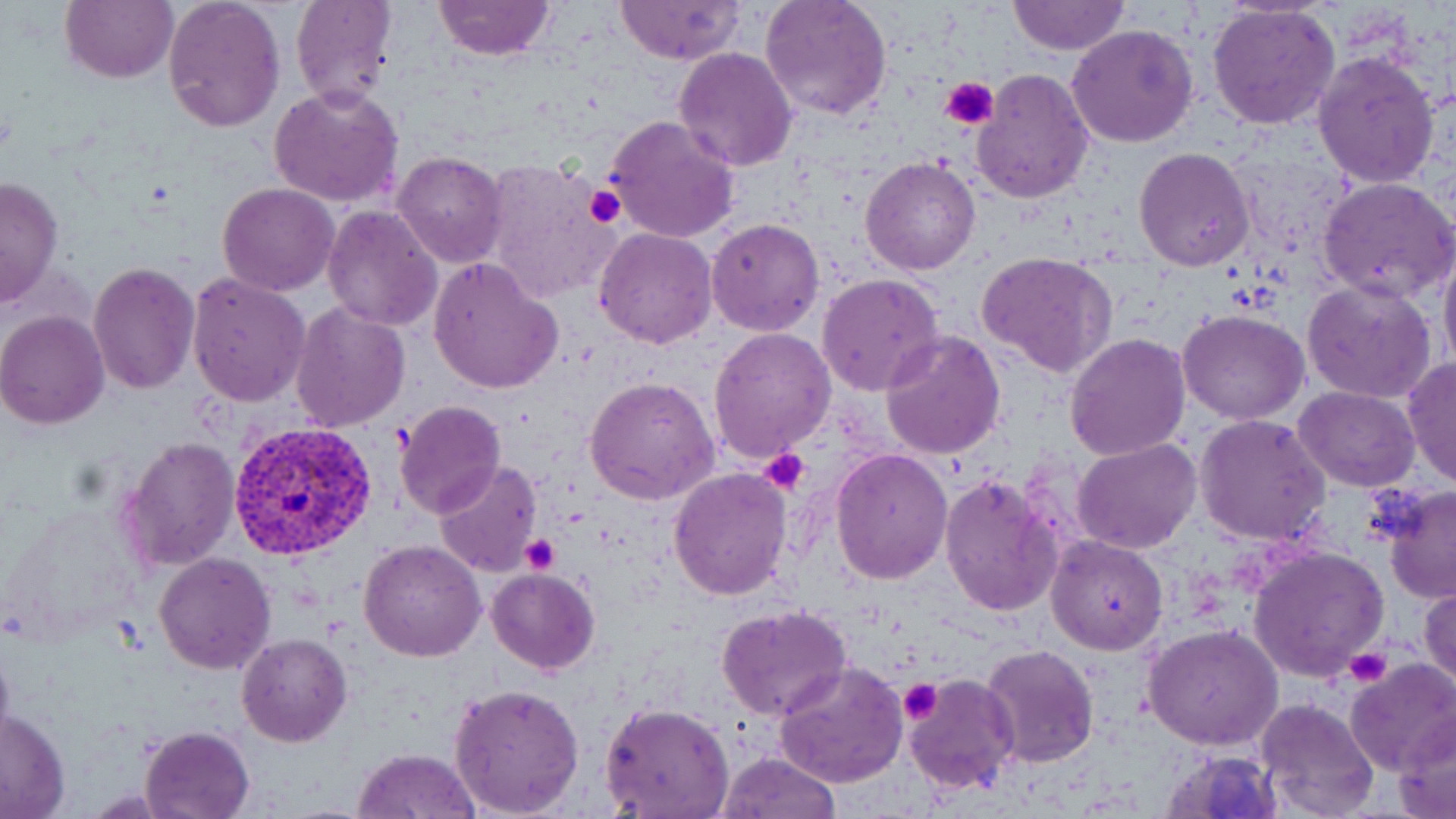

Approximate bounding boxes as (x1, y1, x2, y2) in pixels. Platelet locations: (941, 76, 996, 127), (585, 183, 625, 230), (760, 448, 811, 495), (520, 533, 561, 573), (1345, 646, 1391, 689), (899, 677, 942, 722). Uninfected red blood cell locations: (61, 0, 179, 84), (163, 0, 286, 134), (290, 0, 397, 108), (433, 0, 555, 60), (614, 0, 745, 64), (759, 0, 893, 122), (1007, 0, 1129, 56), (1207, 3, 1340, 132), (1066, 23, 1200, 149), (673, 47, 799, 170), (1312, 52, 1440, 189), (970, 68, 1094, 205), (269, 86, 404, 207), (605, 114, 740, 244), (1134, 147, 1255, 270), (391, 150, 509, 268), (860, 156, 981, 276), (482, 159, 618, 300), (1, 174, 64, 309), (1317, 176, 1456, 303), (217, 182, 341, 296), (321, 204, 445, 331), (706, 217, 824, 338), (594, 227, 717, 348), (1438, 246, 1456, 378), (975, 250, 1118, 377), (428, 257, 564, 395), (87, 259, 200, 396), (186, 272, 310, 407), (816, 274, 945, 396), (1302, 279, 1438, 403), (290, 301, 411, 432), (1178, 309, 1309, 424), (0, 311, 109, 429), (708, 328, 837, 463), (879, 331, 1006, 461), (1065, 332, 1191, 462), (1402, 358, 1455, 488), (584, 375, 718, 505), (1294, 387, 1419, 490), (394, 400, 505, 518), (1194, 413, 1332, 545), (116, 434, 241, 573), (1072, 438, 1201, 553), (830, 450, 952, 585), (435, 460, 542, 576), (669, 466, 793, 599), (940, 473, 1065, 617), (1380, 484, 1455, 604), (1047, 536, 1168, 655), (359, 538, 487, 661), (1248, 547, 1390, 683), (153, 553, 276, 675), (485, 568, 600, 675), (1420, 582, 1456, 691), (716, 605, 852, 721), (1144, 625, 1284, 750), (0, 632, 15, 755), (237, 633, 351, 747), (979, 642, 1102, 768), (1345, 659, 1456, 774), (774, 660, 910, 790), (903, 673, 1020, 795), (449, 682, 586, 816), (1255, 698, 1381, 819), (600, 701, 735, 819), (1, 707, 71, 818), (1395, 710, 1456, 817), (140, 725, 254, 817), (1160, 747, 1282, 819), (352, 748, 480, 819), (716, 752, 840, 819). Plasmodium vivax-infected red blood cell locations: (225, 420, 378, 562). Slide-level diagnosis: Plasmodium vivax. One field of a larger specimen. May-Grünwald-Giemsa stain. Thin blood film. Light microscopy. Captured at 1000x magnification. Image is 1456×819 pixels.